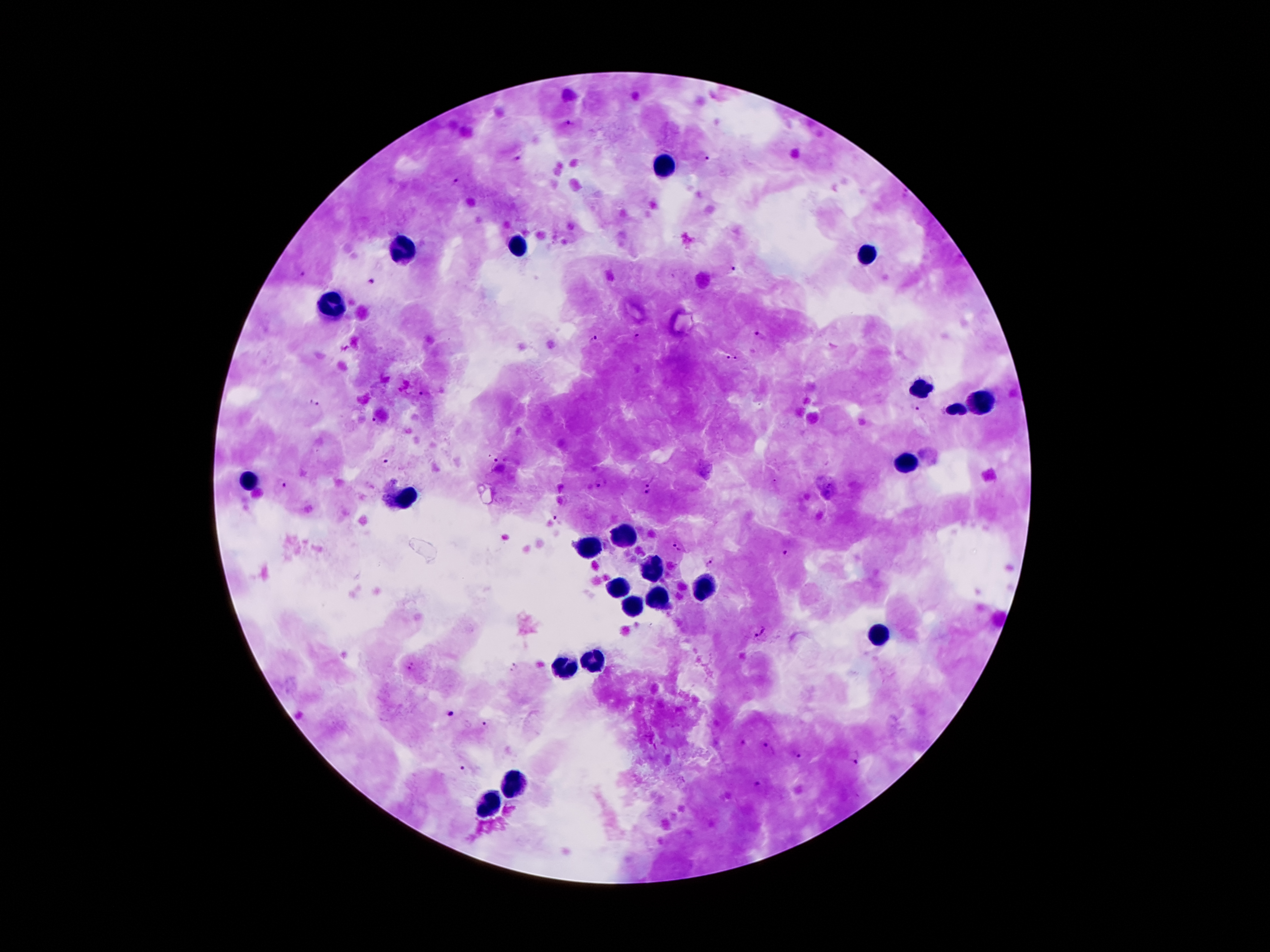
Approximate centers as (x, y) in pixels.
Summary:
  - Leukocyte locations: (662, 164), (514, 245), (404, 251), (865, 254), (330, 306), (919, 392), (975, 403), (955, 409), (904, 465), (253, 478), (404, 495), (621, 534), (585, 551), (649, 571), (615, 590), (703, 590), (656, 600), (630, 607), (876, 631), (593, 659), (565, 668), (514, 783), (488, 804)
  - Plasmodium parasite locations: (568, 123), (520, 157), (707, 158), (459, 180), (731, 268), (300, 273), (372, 280), (760, 335), (637, 336), (593, 339), (727, 356), (737, 359), (423, 394), (313, 401), (914, 409), (373, 420), (497, 460), (385, 462), (649, 481), (600, 482), (281, 486), (649, 497), (557, 519), (676, 548), (787, 554), (710, 562), (762, 631), (410, 666), (450, 714), (487, 724), (744, 744), (769, 749), (796, 754), (855, 756), (462, 769), (760, 787)
  - Patient malaria status: positive for Plasmodium falciparum
  - Magnification: 100x
  - Image size: 1270×952 pixels
  - Stain: Giemsa
  - Field of view: one from this slide
  - Preparation: thick peripheral-blood smear
  - Capture: smartphone through the microscope eyepiece